Give the position of every Plasmodium parasite visible.
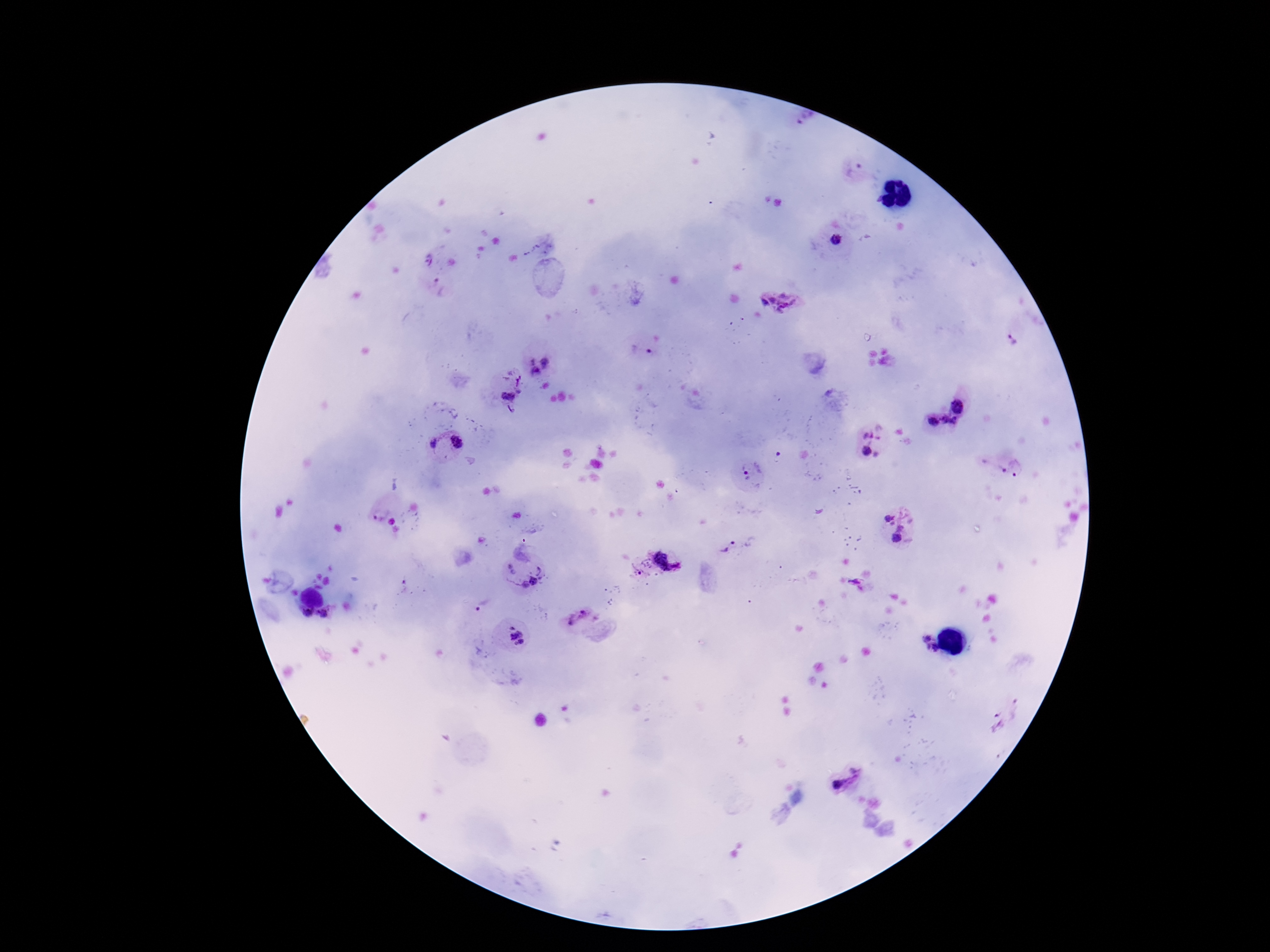

Approximate centers as (x, y) in pixels.
Plasmodium parasites: (805, 120), (856, 172), (838, 241), (778, 302), (1010, 339), (642, 352), (531, 360), (547, 362), (536, 372), (520, 382), (508, 395), (961, 404), (930, 422), (950, 424), (872, 434), (459, 442), (433, 444), (866, 451), (1020, 468), (752, 470), (1003, 470), (380, 513), (889, 519), (900, 527), (897, 538), (729, 547), (670, 554), (639, 568), (512, 570), (542, 570), (855, 581), (532, 582), (484, 606), (306, 613), (323, 615), (583, 617), (517, 636), (927, 639), (929, 647), (936, 648), (999, 723), (855, 769), (838, 784).

Summary:
  - Capture: smartphone camera through the microscope eyepiece
  - Stain: Giemsa
  - Preparation: thick peripheral-blood smear
  - Image size: 1270×952 pixels
  - Field of view: single
  - Patient malaria status: infected
  - Magnification: 100x